State the preparation type.
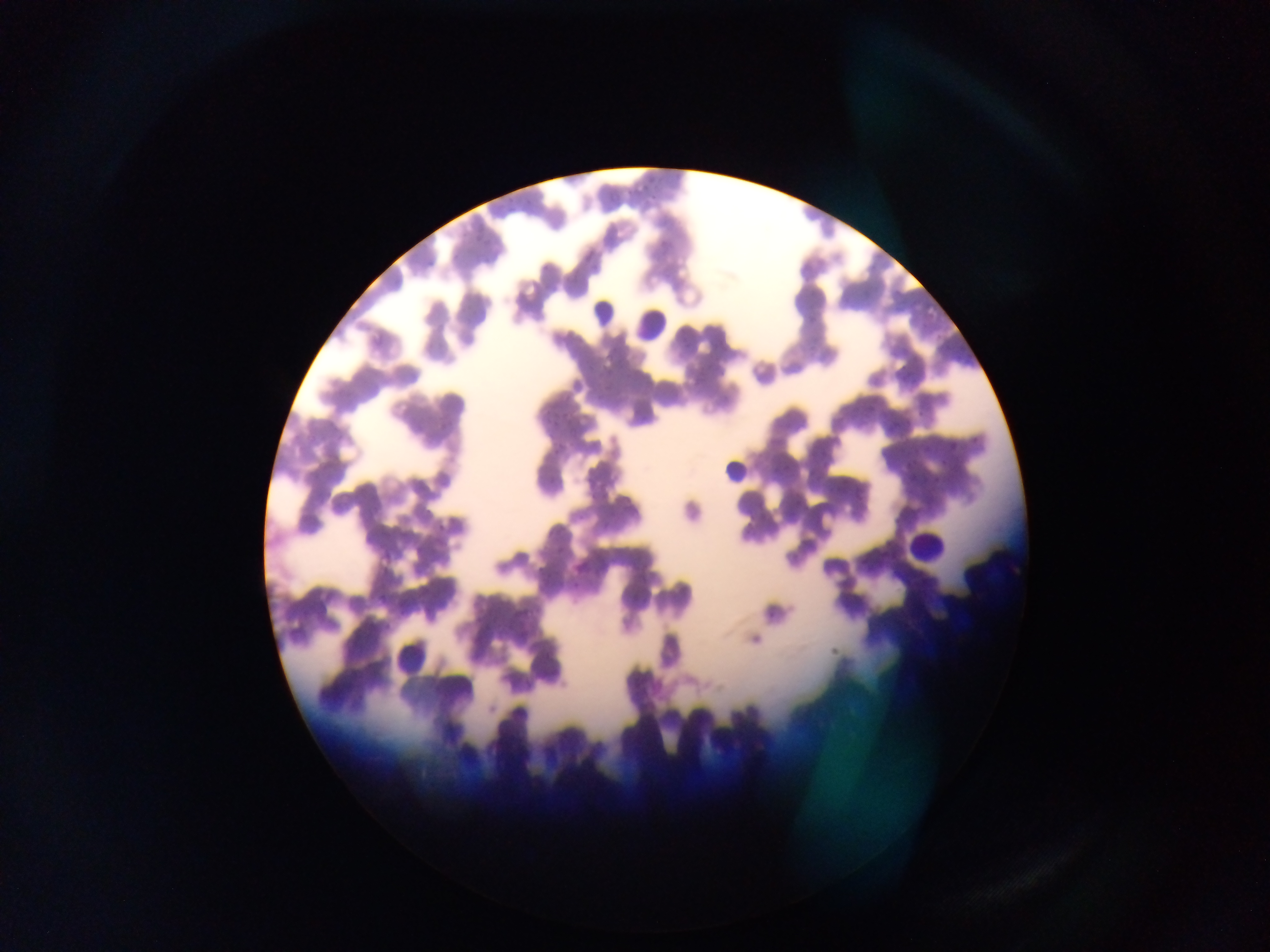
This is a thin smear.

Approximate bounding boxes as [left, top, right, bottom] in pixels.
Summary:
  - Leukocyte locations: [587, 294, 617, 325], [631, 295, 678, 348], [720, 460, 750, 488], [904, 526, 947, 567], [390, 633, 435, 678]
  - Malaria parasite locations: [640, 180, 650, 193], [623, 182, 636, 198], [648, 193, 663, 204], [504, 200, 516, 217], [472, 221, 484, 240], [659, 235, 673, 246], [451, 250, 465, 265], [425, 253, 440, 268], [935, 329, 945, 343], [947, 348, 968, 361], [958, 357, 975, 369], [899, 365, 915, 383], [914, 410, 926, 421], [549, 413, 567, 432], [887, 420, 901, 430], [437, 421, 451, 433], [971, 434, 979, 444], [551, 440, 566, 457], [949, 440, 960, 453], [920, 442, 938, 455], [941, 457, 949, 468], [902, 459, 914, 472], [545, 472, 563, 486], [919, 472, 930, 486], [932, 475, 943, 487], [586, 478, 603, 502], [850, 482, 866, 502], [574, 506, 591, 523], [599, 516, 614, 530], [542, 531, 561, 542], [549, 547, 569, 561], [536, 563, 550, 577], [570, 576, 581, 588], [377, 580, 395, 605], [627, 591, 640, 604], [399, 597, 414, 615]
  - Image size: 1270×952 pixels
  - Country: Ghana
  - Field of view: single
  - Capture: mobile-phone photograph through a microscope